State which parasite is depicted.
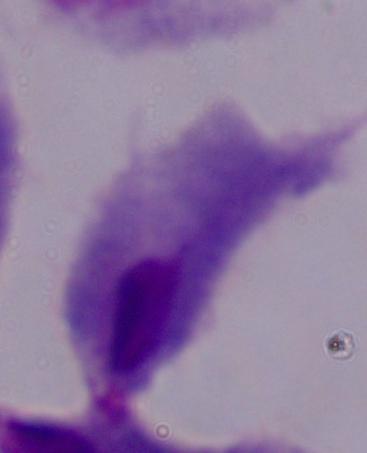

A trichomonad.

modality = micrograph
magnification = 1000x